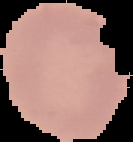

Segmented cell region on a black background. Result: no malaria parasites detected. Image is 133×142 pixels. From a thin blood smear.